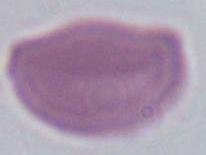

Photomicrograph. A red blood cell is shown. 1000x magnification.